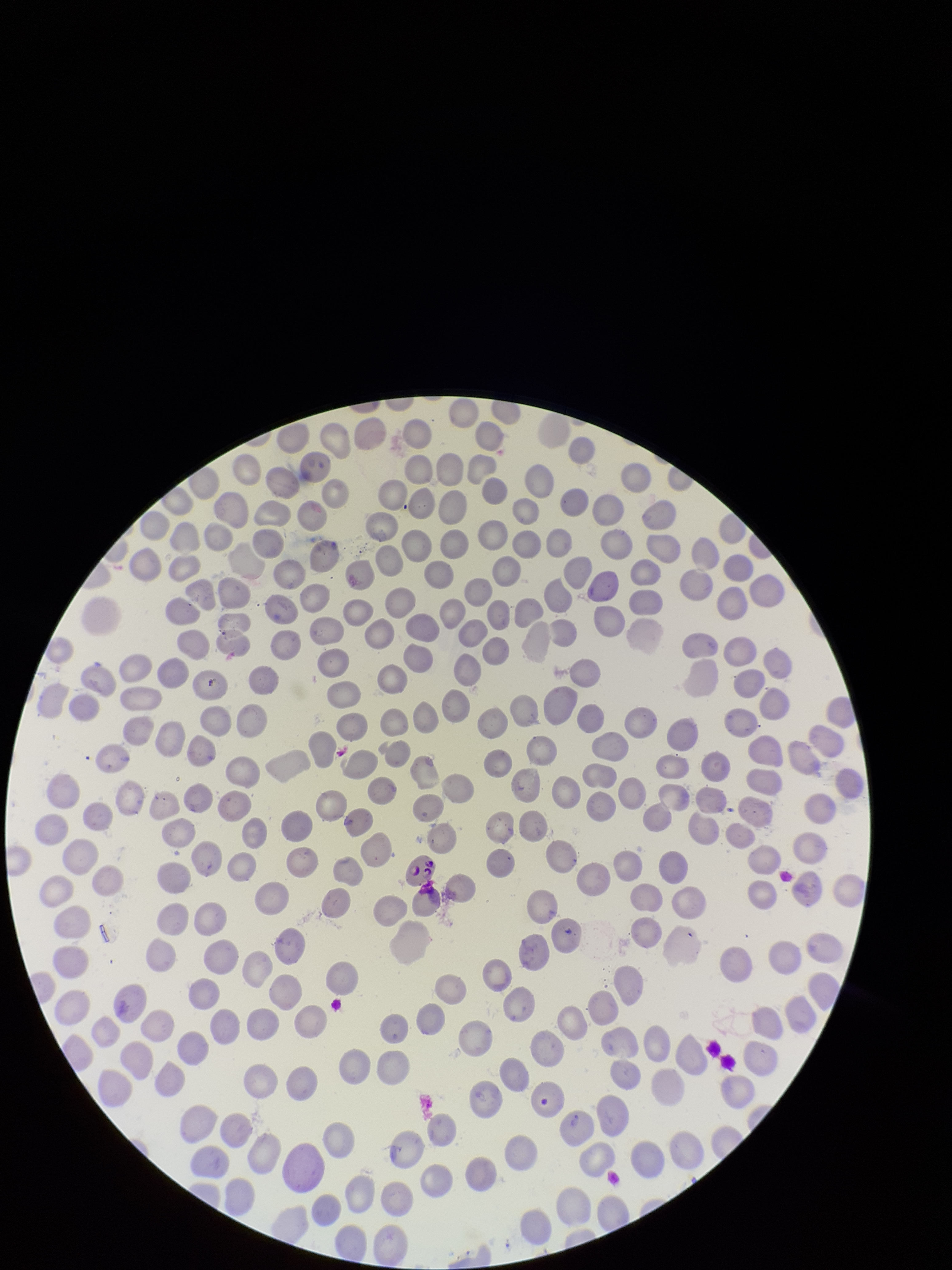

preparation = thin smear
parasitized red blood cell count = 0
species reported for this patient = Plasmodium falciparum
stain = Giemsa
patient malaria status = infected
field of view = one from this slide
image size = 952×1270 pixels
red blood cell count = 279
parasitized red blood cells = none identified
capture = smartphone photograph through the microscope eyepiece